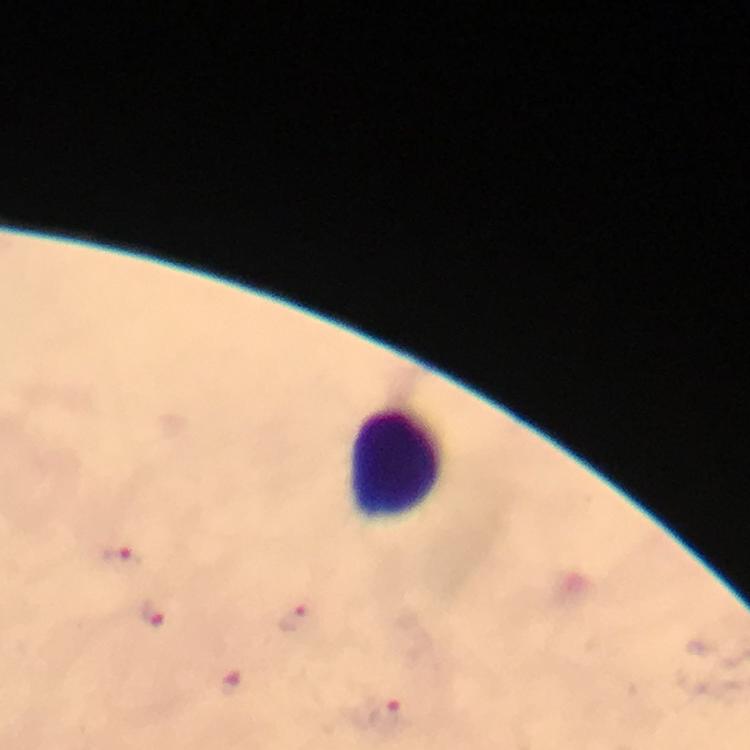
Approximate centers as [x, y] in pixels.
Summary:
  - Plasmodium parasite locations: [122, 556], [156, 612], [295, 616], [230, 679], [389, 717]
  - Leukocyte locations: [396, 464]
  - Cropped from: one field of view
  - Preparation: thick blood smear
  - Image size: 750×750 pixels
  - Context: from a diagnostic examination for malaria
  - Magnification: 100x
  - Stain: Giemsa
  - Immersion oil: used
  - Capture: smartphone mounted on the microscope